Outline every malaria parasite, every leukocyte, and every artifact (stain precipitate or debris).
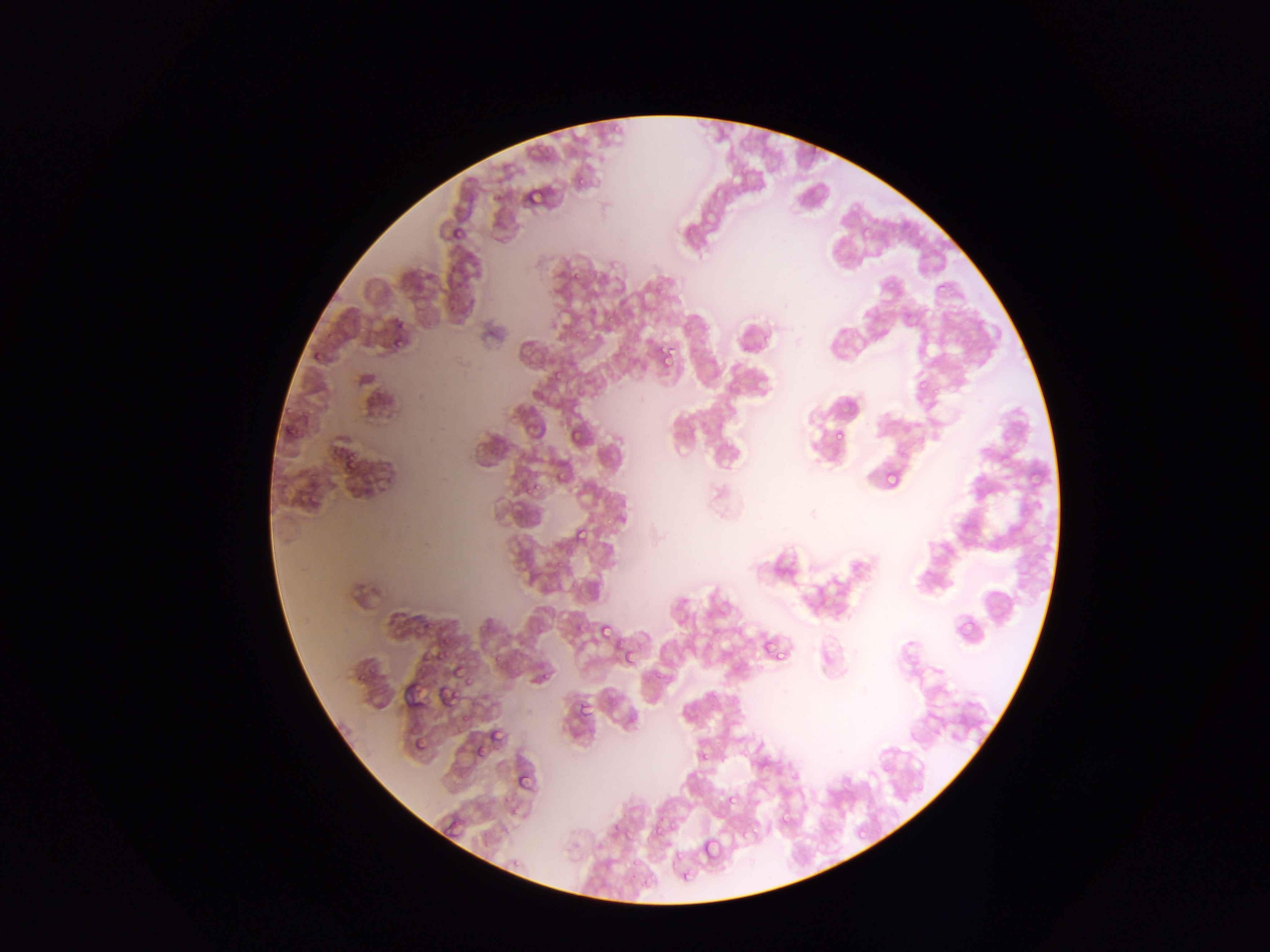
Approximate bounding boxes as [left, top, right, bottom] in pixels.
Malaria parasites: [603, 119, 628, 136], [524, 137, 552, 160], [572, 163, 589, 189], [524, 185, 543, 202], [451, 216, 473, 242], [935, 283, 944, 292], [903, 310, 913, 319], [393, 319, 404, 330], [391, 332, 402, 356], [656, 350, 673, 365], [310, 351, 326, 365], [928, 357, 939, 368], [550, 370, 563, 384], [917, 378, 929, 393], [285, 416, 305, 439], [567, 428, 578, 448], [832, 428, 845, 442], [336, 449, 360, 471], [999, 449, 1013, 462], [885, 470, 902, 487], [520, 476, 540, 492], [304, 482, 325, 505], [574, 525, 590, 543], [557, 559, 563, 567], [956, 616, 975, 637], [597, 623, 612, 639], [760, 638, 774, 653], [765, 640, 783, 658], [429, 648, 443, 665], [623, 648, 636, 663], [450, 666, 463, 679], [466, 674, 480, 691], [443, 685, 459, 702], [576, 701, 589, 715], [494, 732, 515, 740], [411, 735, 428, 751], [473, 742, 486, 755], [697, 749, 709, 762], [519, 774, 533, 791], [726, 793, 736, 808], [778, 814, 792, 828], [650, 819, 668, 839], [856, 825, 867, 836], [617, 826, 634, 845], [700, 837, 721, 859], [667, 851, 684, 869], [624, 859, 645, 870], [683, 865, 698, 881], [640, 868, 660, 892].
No leukocytes observed.

country: Ghana
field_of_view: single
capture: mobile-phone photograph through a microscope
preparation: thin blood smear
image_size: 1270×952 pixels